Classify this cell by malaria status.
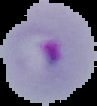
Parasitized.

image type = segmented cell region on a black background
preparation = thin blood film
image size = 97×106 pixels